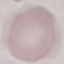

malaria status = uninfected
stain = Giemsa
preparation = thin smear
capture = smartphone through the microscope eyepiece
image type = cell patch, automatically extracted from a larger field of view and resized to 64 × 64 pixels